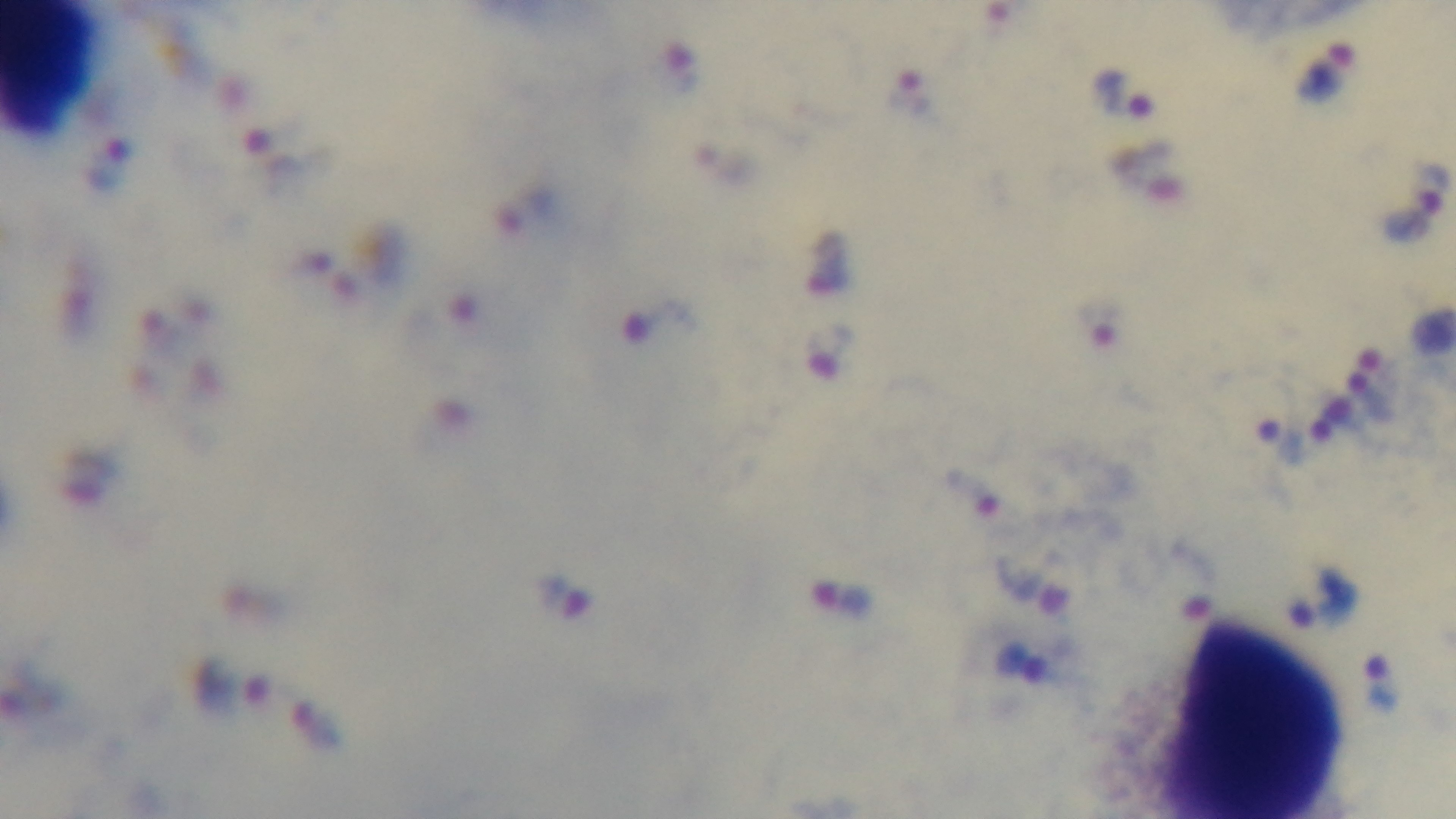 Photomicrograph. Mounted 4K digital camera. Giemsa stain. One field from the slide. Malaria status: infected. Oil-immersion objective, 100x. Preparation: thick blood film.